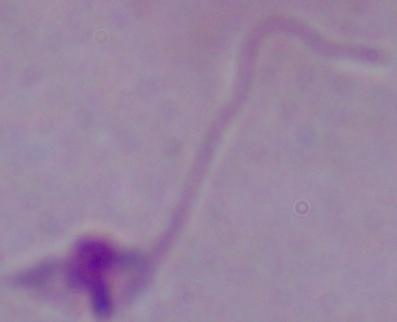

A Leishmania parasite is seen. Micrograph. Captured at 1000x magnification.